State the blood parasite species.
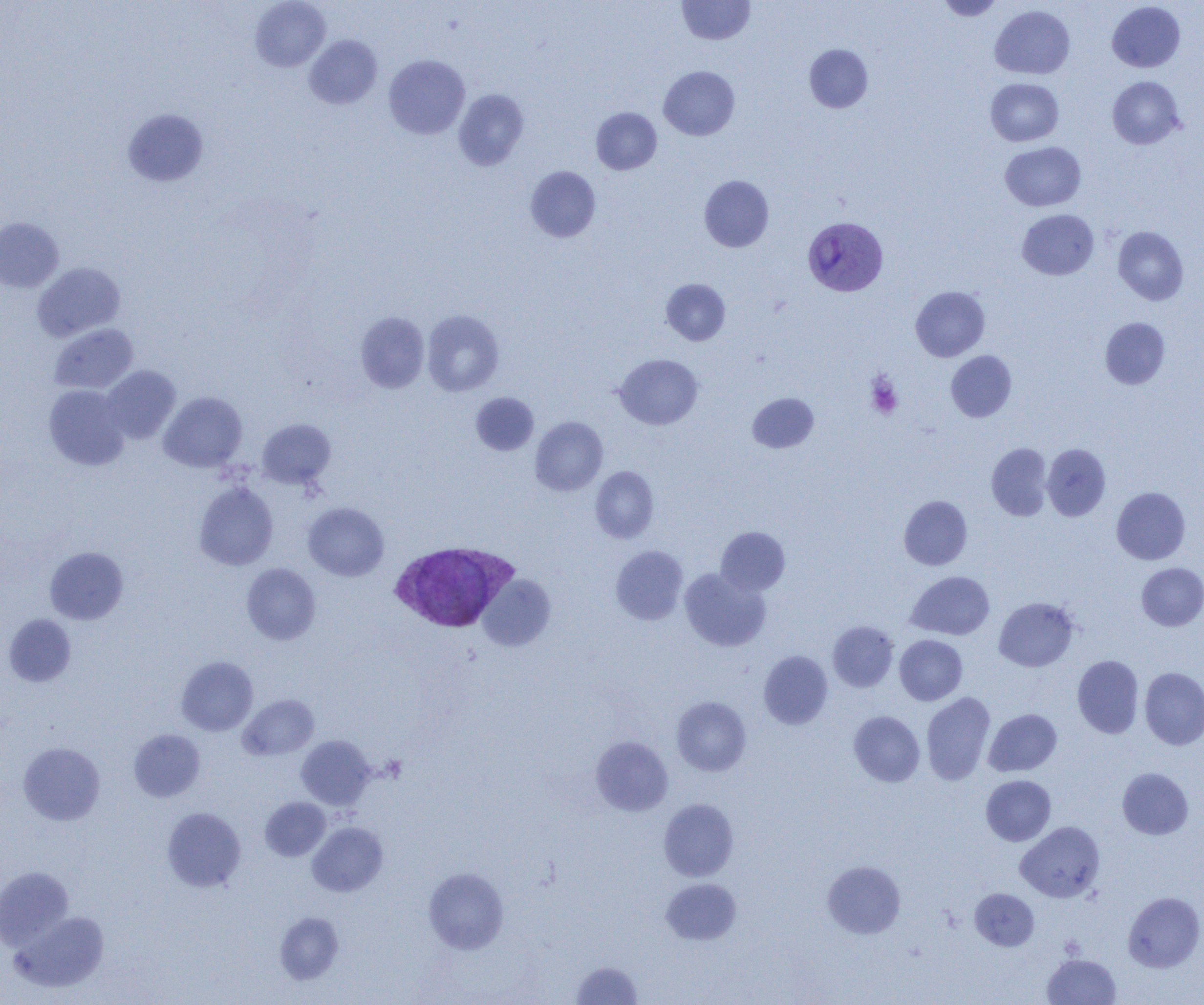
Plasmodium vivax.

magnification = 1000x
image size = 1204×1005 pixels
Plasmodium vivax-infected red blood cell locations = approximate bounding boxes as named x1/y1/x2/y2 corners in pixels: (x1=803, y1=216, x2=888, y2=296), (x1=389, y1=540, x2=518, y2=633)
field of view = one of a larger specimen
modality = optical microscopy
preparation = thin blood film
platelet locations = approximate bounding boxes as named x1/y1/x2/y2 corners in pixels: (x1=866, y1=374, x2=903, y2=419)
uninfected red blood cell locations = approximate bounding boxes as named x1/y1/x2/y2 corners in pixels: (x1=250, y1=0, x2=330, y2=71), (x1=677, y1=0, x2=755, y2=45), (x1=937, y1=0, x2=1004, y2=20), (x1=1107, y1=1, x2=1185, y2=72), (x1=990, y1=5, x2=1075, y2=79), (x1=304, y1=35, x2=382, y2=109), (x1=804, y1=44, x2=873, y2=113), (x1=384, y1=54, x2=470, y2=139), (x1=658, y1=66, x2=740, y2=140), (x1=1107, y1=76, x2=1185, y2=149), (x1=985, y1=78, x2=1064, y2=146), (x1=453, y1=89, x2=529, y2=170), (x1=591, y1=107, x2=661, y2=174), (x1=122, y1=108, x2=209, y2=187), (x1=1000, y1=142, x2=1086, y2=211), (x1=525, y1=166, x2=600, y2=242), (x1=699, y1=175, x2=774, y2=252), (x1=1017, y1=209, x2=1098, y2=279), (x1=0, y1=217, x2=64, y2=293), (x1=1113, y1=226, x2=1188, y2=305), (x1=32, y1=262, x2=125, y2=341), (x1=661, y1=278, x2=730, y2=346), (x1=911, y1=286, x2=990, y2=361), (x1=422, y1=310, x2=504, y2=396), (x1=356, y1=312, x2=429, y2=393), (x1=1100, y1=317, x2=1170, y2=389), (x1=49, y1=324, x2=139, y2=394), (x1=946, y1=350, x2=1017, y2=421), (x1=614, y1=353, x2=702, y2=429), (x1=102, y1=365, x2=181, y2=444), (x1=44, y1=385, x2=130, y2=471), (x1=158, y1=391, x2=247, y2=472), (x1=471, y1=393, x2=539, y2=455), (x1=747, y1=393, x2=818, y2=453), (x1=530, y1=417, x2=608, y2=495), (x1=257, y1=418, x2=336, y2=489), (x1=987, y1=443, x2=1052, y2=520), (x1=1042, y1=443, x2=1111, y2=521), (x1=590, y1=466, x2=659, y2=543), (x1=194, y1=482, x2=278, y2=570), (x1=1111, y1=486, x2=1191, y2=564), (x1=899, y1=495, x2=972, y2=570), (x1=303, y1=502, x2=389, y2=581), (x1=716, y1=526, x2=790, y2=596), (x1=610, y1=545, x2=688, y2=625), (x1=45, y1=546, x2=128, y2=625), (x1=1136, y1=562, x2=1204, y2=631), (x1=241, y1=563, x2=320, y2=645), (x1=679, y1=568, x2=770, y2=651), (x1=907, y1=571, x2=994, y2=640), (x1=478, y1=574, x2=555, y2=651), (x1=994, y1=597, x2=1079, y2=671), (x1=3, y1=614, x2=77, y2=687), (x1=828, y1=621, x2=898, y2=692), (x1=895, y1=635, x2=967, y2=705), (x1=759, y1=650, x2=833, y2=729), (x1=1072, y1=655, x2=1144, y2=738), (x1=176, y1=656, x2=258, y2=735), (x1=1140, y1=667, x2=1204, y2=750), (x1=921, y1=692, x2=995, y2=785), (x1=238, y1=694, x2=319, y2=761), (x1=671, y1=696, x2=751, y2=776), (x1=983, y1=708, x2=1062, y2=776), (x1=849, y1=711, x2=925, y2=786), (x1=128, y1=729, x2=205, y2=802), (x1=296, y1=735, x2=376, y2=810), (x1=591, y1=736, x2=673, y2=816), (x1=19, y1=742, x2=105, y2=825), (x1=1117, y1=767, x2=1193, y2=840), (x1=981, y1=775, x2=1055, y2=846), (x1=260, y1=797, x2=331, y2=861), (x1=659, y1=798, x2=739, y2=881), (x1=162, y1=807, x2=246, y2=892), (x1=1016, y1=821, x2=1105, y2=902), (x1=307, y1=822, x2=388, y2=897), (x1=822, y1=860, x2=906, y2=938), (x1=0, y1=867, x2=74, y2=950), (x1=423, y1=867, x2=508, y2=954), (x1=661, y1=878, x2=741, y2=944), (x1=970, y1=888, x2=1039, y2=950), (x1=1123, y1=892, x2=1204, y2=972), (x1=12, y1=911, x2=110, y2=992), (x1=275, y1=912, x2=344, y2=984), (x1=1042, y1=953, x2=1121, y2=1004), (x1=571, y1=961, x2=642, y2=1004)